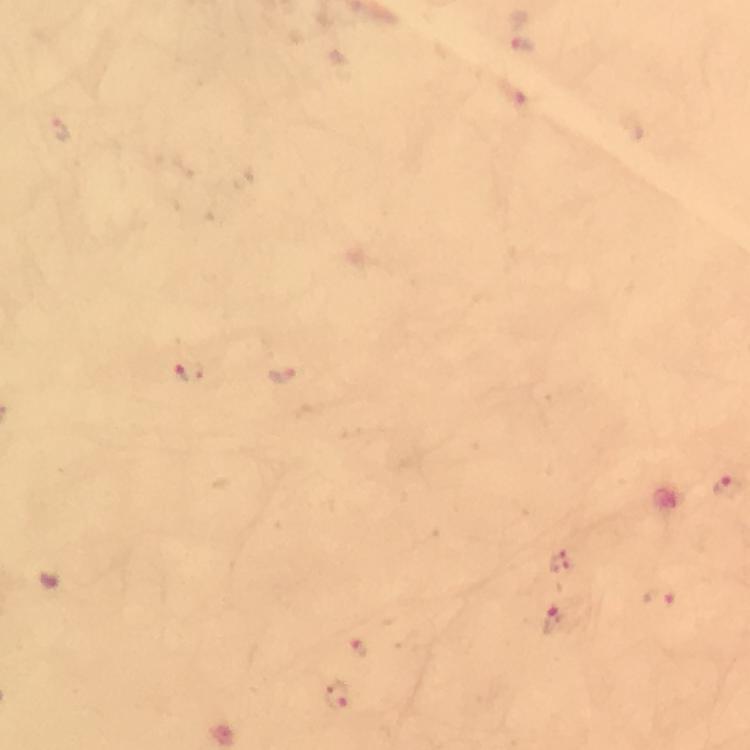 Approximate object centers, in pixels from the top-left corner. Plasmodium parasite locations: (x=522, y=44), (x=190, y=373), (x=283, y=378), (x=726, y=486), (x=559, y=561), (x=659, y=599), (x=555, y=619), (x=360, y=647), (x=336, y=696). A crop from one field of view. From a malaria diagnostic workup. Thick blood film. Image is 750×750 pixels. Giemsa-stained preparation. Photographed with a smartphone mounted on the microscope. Immersion oil applied. At 100x magnification.